Locate every Plasmodium falciparum-infected red blood cell.
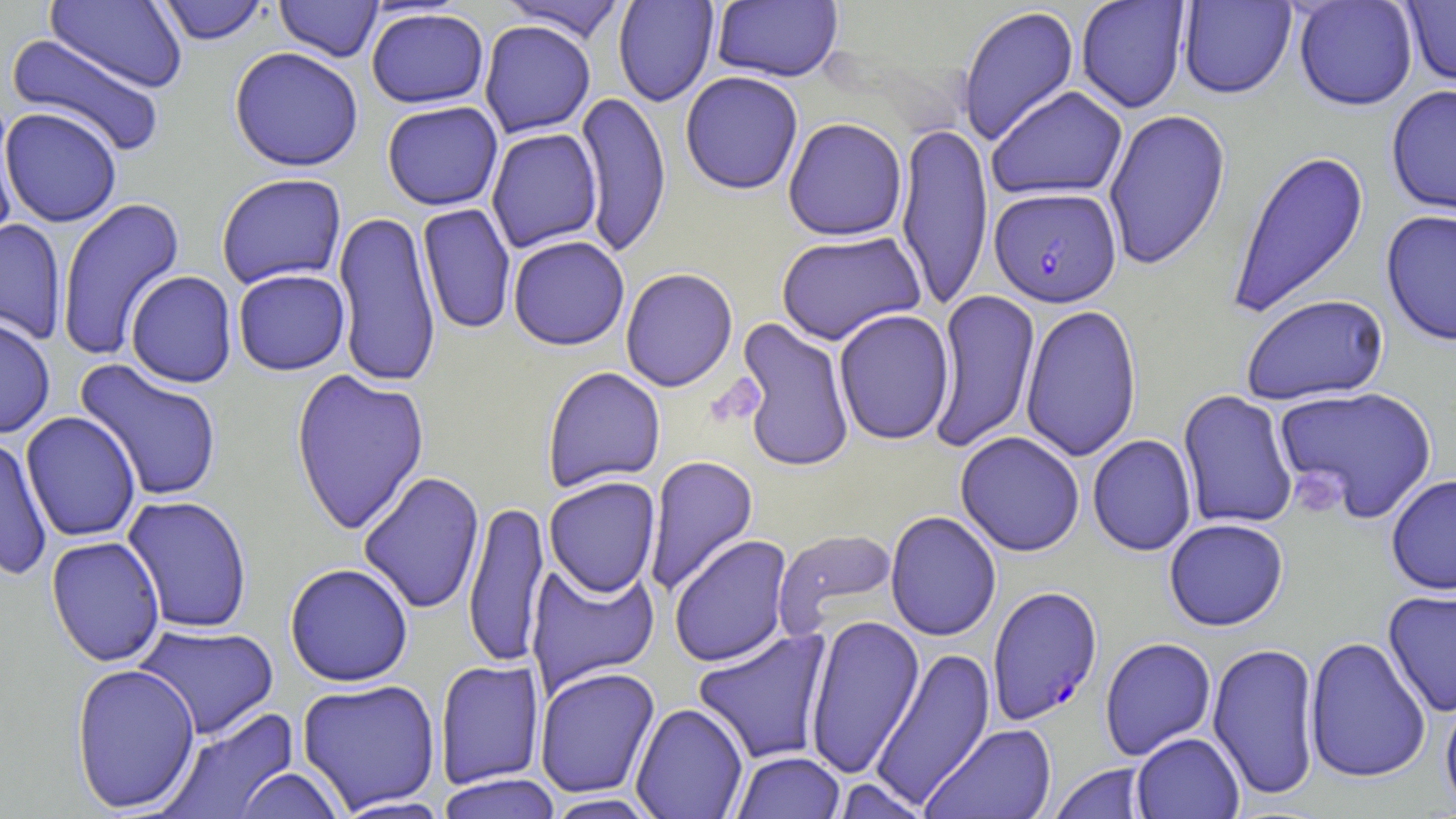
Approximate bounding boxes as (x1,y1)-(x2,y2) corner pairs in pixels.
Plasmodium falciparum-infected red blood cells: (989,187)-(1122,307), (987,584)-(1103,725).

Summary:
  - Uninfected red blood cell locations: (46,0)-(188,93), (154,0)-(271,45), (497,0)-(629,42), (612,0)-(719,108), (1075,0)-(1191,114), (1293,0)-(1418,112), (1401,0)-(1456,90), (274,1)-(383,62), (711,1)-(843,83), (1178,1)-(1297,100), (957,5)-(1080,147), (366,7)-(489,109), (479,20)-(596,138), (5,34)-(168,158), (228,47)-(364,172), (680,71)-(803,195), (1385,84)-(1456,220), (986,86)-(1128,201), (0,92)-(20,247), (575,92)-(672,259), (381,101)-(504,211), (0,107)-(123,228), (1103,108)-(1231,270), (782,117)-(907,241), (895,119)-(993,313), (486,128)-(603,253), (1227,148)-(1370,319), (216,173)-(347,289), (55,196)-(186,362), (417,203)-(517,336), (333,210)-(441,388), (1381,210)-(1456,346), (0,218)-(67,345), (776,231)-(927,345), (507,235)-(630,351), (620,267)-(738,392), (233,268)-(350,376), (125,270)-(237,388), (929,288)-(1041,453), (1240,294)-(1390,406), (1020,303)-(1142,462), (833,309)-(955,445), (0,316)-(56,438), (733,317)-(856,473), (74,359)-(224,502), (541,367)-(666,493), (290,368)-(430,536), (1274,385)-(1439,524), (1177,390)-(1299,531), (21,412)-(141,543), (955,431)-(1085,557), (1087,434)-(1197,556), (0,435)-(54,581), (643,454)-(760,597), (358,471)-(485,614), (1385,473)-(1456,595), (543,476)-(661,598), (122,495)-(253,634), (463,499)-(549,669), (885,511)-(1001,642), (1163,518)-(1289,631), (772,528)-(899,637), (668,534)-(794,668), (46,535)-(166,667), (525,560)-(661,695), (284,563)-(414,687), (1382,588)-(1456,717), (805,614)-(925,779), (133,624)-(279,740), (692,628)-(834,765), (1304,635)-(1432,784), (1099,637)-(1216,760), (1207,641)-(1321,801), (870,646)-(996,807), (434,658)-(545,790), (69,662)-(201,813), (534,666)-(660,799), (296,678)-(442,813), (1440,690)-(1456,815), (630,703)-(749,818), (157,706)-(301,819), (920,723)-(1058,818), (1131,732)-(1245,819), (730,751)-(846,819), (1048,763)-(1153,819), (233,767)-(348,818), (435,773)-(563,819), (831,777)-(932,819), (542,793)-(662,819), (331,795)-(455,818)
  - Platelet locations: (1291,469)-(1345,519)
  - Slide-level diagnosis: Plasmodium falciparum
  - Field of view: single
  - Stain: May-Grünwald-Giemsa
  - Magnification: 1000x
  - Modality: optical microscopy
  - Preparation: thin blood smear
  - Image size: 1456×819 pixels